Report the malaria status of this cell.
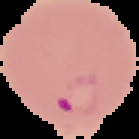
Parasitized.

Summary:
  - Image type: cell region segmented out of the field of view; surrounding area masked to black
  - Preparation: thin blood smear
  - Image size: 139×139 pixels